Name the parasite shown.
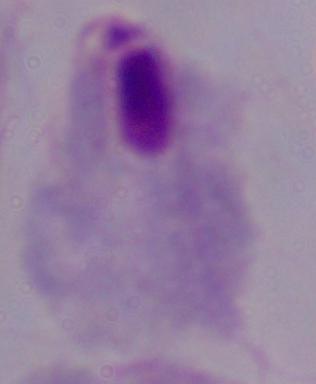

This is a trichomonad.

{
  "magnification": "1000x",
  "modality": "micrograph"
}